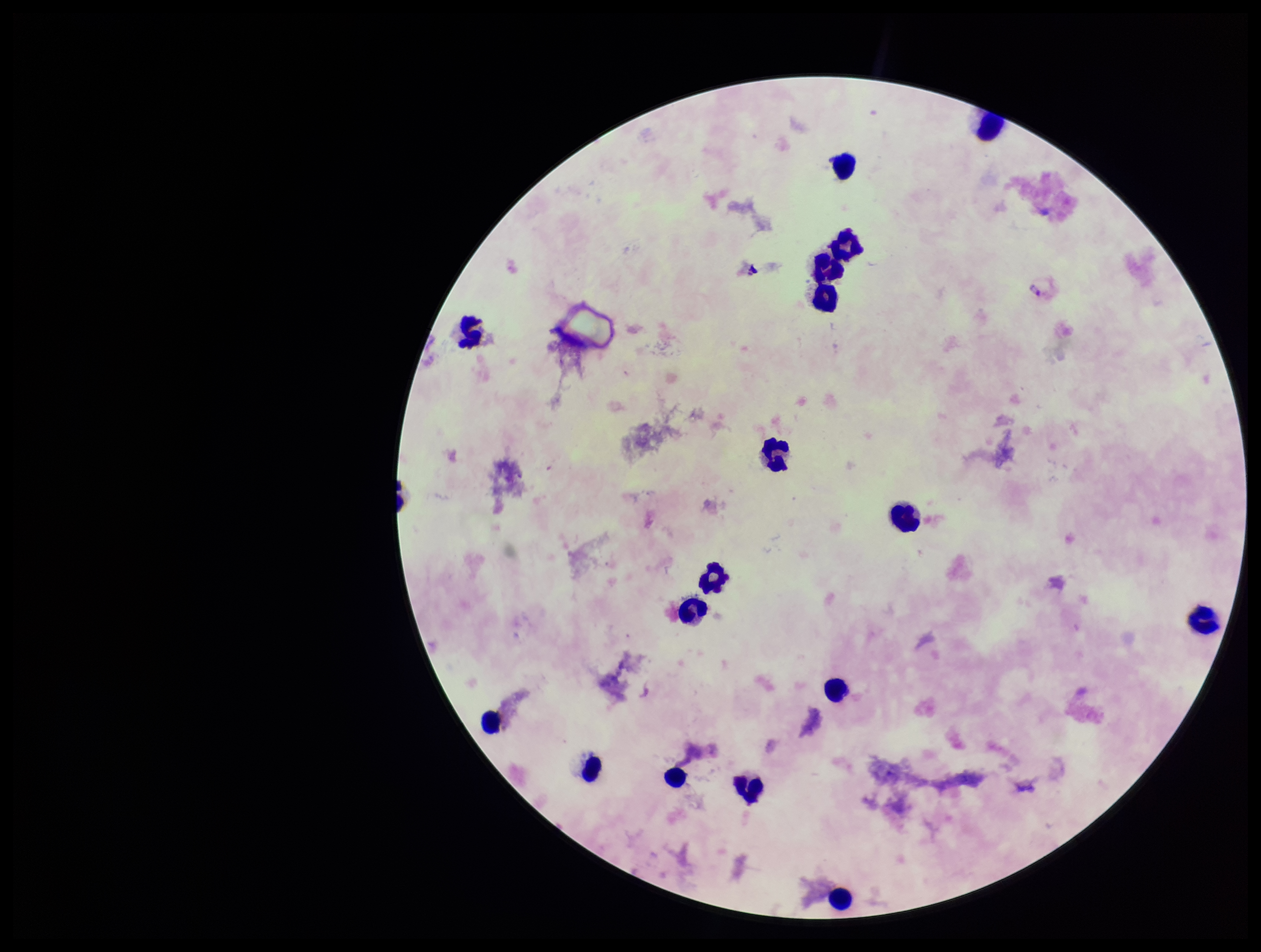

Summary:
  - Preparation: thick smear
  - Parasite count: 1
  - Image size: 1261×952 pixels
  - Field of view: single
  - Plasmodium parasites: detected
  - Capture: smartphone photograph through the microscope eyepiece
  - Leukocyte count: 17
  - Patient malaria status: infected
  - Stain: Giemsa
  - Species reported for this patient: Plasmodium vivax